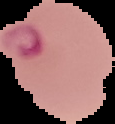
image type = cell region segmented out of the field of view; surrounding area masked to black
image size = 115×124 pixels
malaria status = parasitized
preparation = thin blood film